Identify the preparation type.
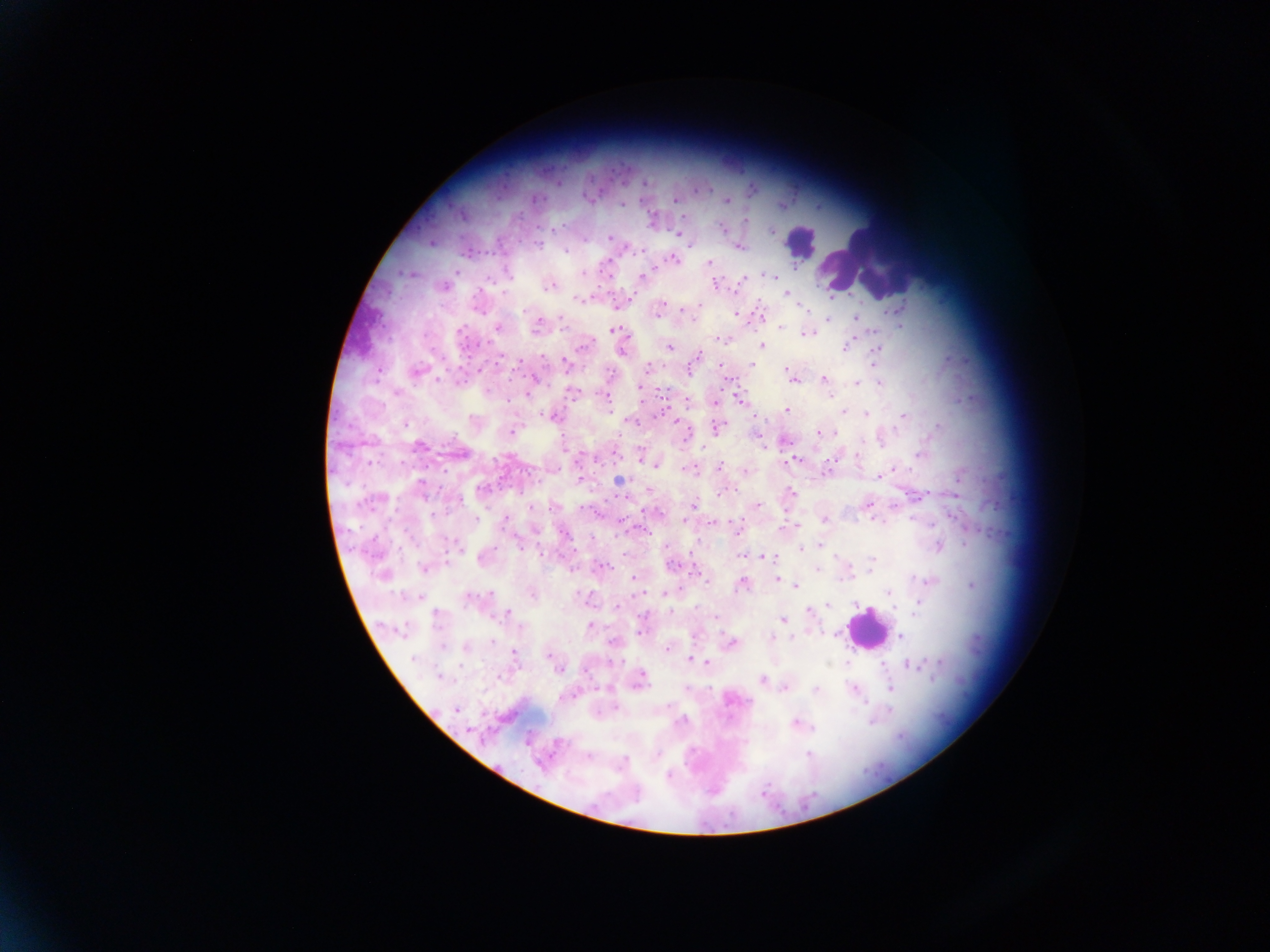

This is a thick smear.

image size = 1270×952 pixels
country = Ghana
field of view = single
leukocyte locations = approximate centers as {x, y} in pixels: {799, 242}, {862, 258}, {866, 628}
Plasmodium parasite locations = approximate centers as {x, y} in pixels: {557, 183}, {644, 184}, {751, 189}, {588, 198}, {674, 200}, {727, 201}, {622, 203}, {782, 205}, {686, 217}, {652, 220}, {744, 221}, {723, 230}, {771, 231}, {678, 234}, {609, 237}, {431, 242}, {691, 245}, {738, 247}, {565, 250}, {623, 250}, {466, 253}, {672, 258}, {710, 263}, {456, 271}, {583, 273}, {608, 274}, {770, 275}, {642, 277}, {742, 279}, {716, 283}, {550, 284}, {740, 284}, {443, 287}, {787, 293}, {631, 298}, {579, 299}, {616, 304}, {699, 304}, {802, 306}, {901, 307}, {886, 311}, {658, 312}, {735, 314}, {761, 316}, {855, 318}, {828, 319}, {693, 321}, {537, 324}, {902, 327}, {497, 328}, {780, 328}, {616, 330}, {806, 333}, {724, 341}, {584, 345}, {669, 346}, {762, 346}, {846, 347}, {876, 349}, {623, 351}, {697, 356}, {566, 363}, {752, 365}, {648, 367}, {415, 372}, {533, 376}, {792, 378}, {823, 378}, {855, 384}, {879, 384}, {640, 387}, {572, 392}, {527, 393}, {829, 393}, {738, 397}, {687, 402}, {714, 403}, {787, 410}, {843, 411}, {866, 414}, {551, 415}, {758, 415}, {903, 416}, {404, 423}, {717, 427}, {820, 431}, {511, 433}, {836, 433}, {685, 434}, {758, 435}, {783, 440}, {419, 445}, {702, 447}, {764, 448}, {458, 452}, {640, 454}, {919, 455}, {794, 459}, {789, 462}, {657, 464}, {720, 466}, {691, 469}, {893, 469}, {744, 472}, {827, 472}, {878, 476}, {580, 480}, {618, 480}, {649, 489}, {718, 493}, {792, 494}, {694, 504}, {757, 504}, {866, 504}, {552, 506}, {476, 519}, {824, 519}, {872, 519}, {685, 520}, {505, 521}, {712, 522}, {738, 527}, {796, 528}, {564, 533}, {820, 545}, {938, 545}, {665, 546}, {458, 547}, {799, 549}, {574, 553}, {741, 556}, {762, 556}, {483, 557}, {871, 561}, {672, 565}, {424, 567}, {602, 567}, {816, 569}, {696, 574}, {384, 575}, {634, 576}, {776, 578}, {708, 581}, {929, 581}, {742, 583}, {972, 584}, {797, 585}, {889, 591}, {532, 593}, {642, 593}, {664, 593}, {417, 596}, {829, 605}, {615, 606}, {915, 610}, {808, 612}, {509, 614}, {436, 615}, {783, 619}, {589, 626}, {641, 632}, {900, 636}, {771, 637}, {730, 644}, {465, 645}, {667, 647}, {513, 653}, {551, 654}, {555, 660}, {690, 660}, {939, 662}, {707, 663}, {911, 664}, {558, 669}, {440, 677}, {762, 680}, {639, 681}, {785, 688}, {853, 688}, {890, 688}, {816, 690}, {731, 698}, {455, 708}, {795, 724}, {809, 755}, {588, 756}, {668, 775}, {713, 789}
capture = mobile-phone photograph through a microscope